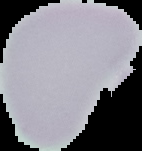

preparation: thin blood film
malaria_status: uninfected
image_type: segmented cell region with the area outside set to black
image_size: 142×151 pixels